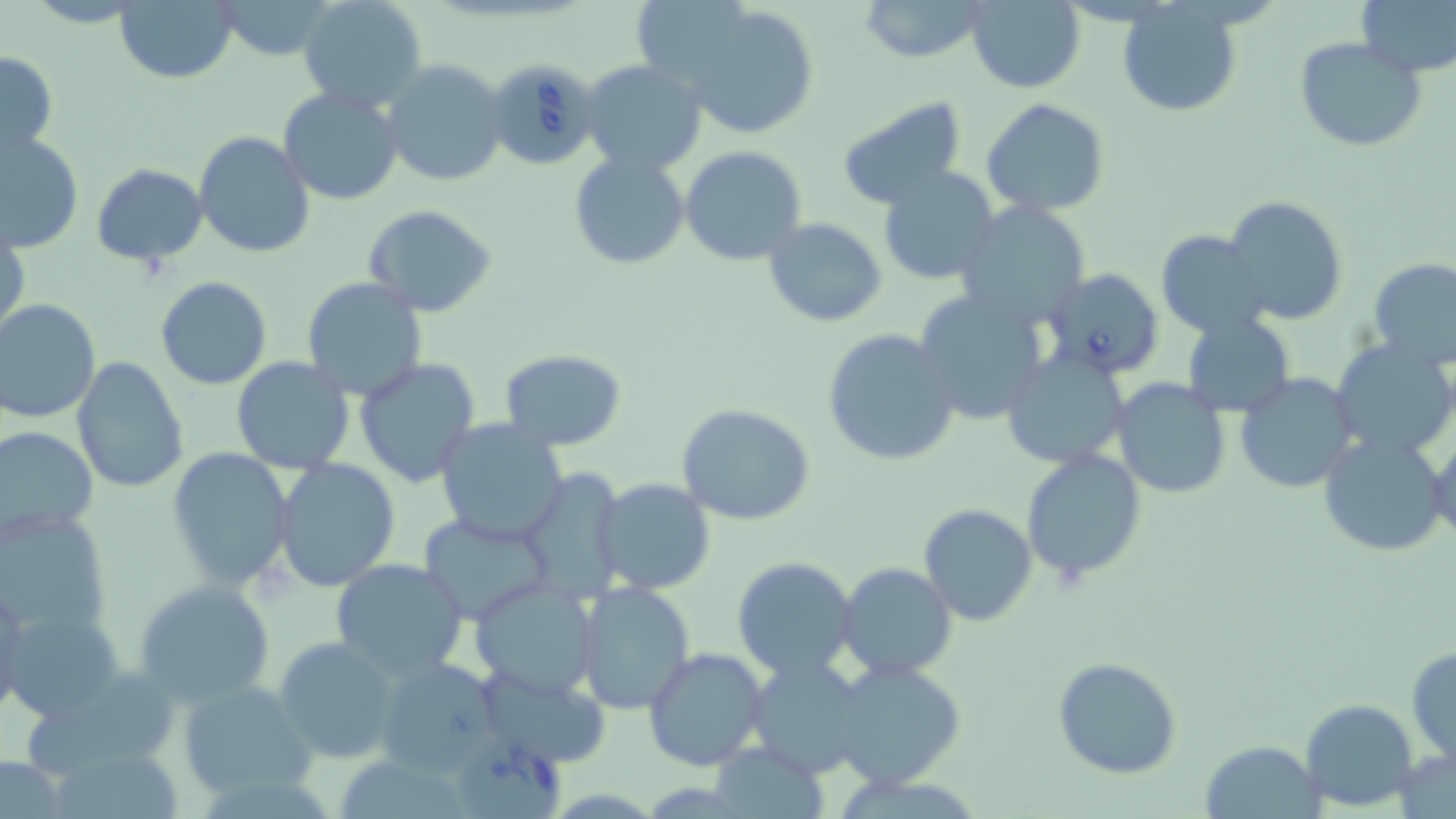
Approximate bounding boxes as named x1/y1/x2/y2 corners in pixels. Uninfected red blood cell locations: (x1=114, y1=0, x2=239, y2=83), (x1=214, y1=0, x2=340, y2=60), (x1=298, y1=0, x2=429, y2=114), (x1=859, y1=0, x2=989, y2=64), (x1=967, y1=0, x2=1086, y2=93), (x1=1358, y1=0, x2=1456, y2=77), (x1=1118, y1=4, x2=1242, y2=119), (x1=682, y1=5, x2=821, y2=138), (x1=1295, y1=37, x2=1426, y2=152), (x1=0, y1=48, x2=59, y2=162), (x1=380, y1=59, x2=508, y2=188), (x1=579, y1=59, x2=707, y2=177), (x1=279, y1=87, x2=403, y2=205), (x1=836, y1=97, x2=967, y2=211), (x1=981, y1=98, x2=1110, y2=219), (x1=193, y1=131, x2=314, y2=258), (x1=1, y1=133, x2=84, y2=253), (x1=681, y1=145, x2=807, y2=267), (x1=568, y1=150, x2=690, y2=268), (x1=92, y1=162, x2=207, y2=266), (x1=877, y1=165, x2=1001, y2=287), (x1=1224, y1=195, x2=1348, y2=324), (x1=955, y1=203, x2=1092, y2=326), (x1=361, y1=204, x2=496, y2=316), (x1=762, y1=217, x2=887, y2=328), (x1=1, y1=226, x2=28, y2=340), (x1=1156, y1=230, x2=1271, y2=339), (x1=1368, y1=256, x2=1456, y2=370), (x1=154, y1=276, x2=271, y2=389), (x1=302, y1=278, x2=429, y2=402), (x1=913, y1=290, x2=1049, y2=426), (x1=0, y1=299, x2=103, y2=422), (x1=1183, y1=313, x2=1295, y2=418), (x1=821, y1=327, x2=961, y2=466), (x1=1331, y1=339, x2=1456, y2=459), (x1=499, y1=349, x2=628, y2=452), (x1=1000, y1=350, x2=1132, y2=469), (x1=71, y1=357, x2=187, y2=493), (x1=354, y1=357, x2=482, y2=489), (x1=231, y1=358, x2=356, y2=474), (x1=1234, y1=373, x2=1361, y2=493), (x1=1111, y1=379, x2=1232, y2=498), (x1=677, y1=403, x2=816, y2=526), (x1=434, y1=417, x2=569, y2=546), (x1=0, y1=426, x2=99, y2=542), (x1=1317, y1=432, x2=1450, y2=558), (x1=1429, y1=434, x2=1456, y2=544), (x1=169, y1=448, x2=295, y2=592), (x1=1022, y1=449, x2=1147, y2=583), (x1=272, y1=458, x2=401, y2=591), (x1=516, y1=469, x2=627, y2=602), (x1=591, y1=478, x2=716, y2=596), (x1=0, y1=503, x2=111, y2=639), (x1=919, y1=503, x2=1037, y2=626), (x1=418, y1=512, x2=554, y2=624), (x1=731, y1=556, x2=857, y2=680), (x1=330, y1=559, x2=470, y2=679), (x1=835, y1=563, x2=957, y2=680), (x1=133, y1=578, x2=274, y2=705), (x1=467, y1=580, x2=602, y2=701), (x1=0, y1=581, x2=25, y2=723), (x1=574, y1=581, x2=697, y2=713), (x1=3, y1=606, x2=126, y2=723), (x1=273, y1=635, x2=403, y2=764), (x1=643, y1=646, x2=768, y2=772), (x1=1407, y1=648, x2=1455, y2=761), (x1=371, y1=653, x2=501, y2=775), (x1=747, y1=655, x2=872, y2=778), (x1=1052, y1=657, x2=1182, y2=778), (x1=830, y1=659, x2=964, y2=788), (x1=27, y1=662, x2=185, y2=779), (x1=470, y1=662, x2=613, y2=770), (x1=176, y1=677, x2=315, y2=803), (x1=1301, y1=698, x2=1418, y2=810), (x1=1201, y1=738, x2=1322, y2=817), (x1=710, y1=745, x2=832, y2=818), (x1=56, y1=752, x2=181, y2=819), (x1=343, y1=753, x2=466, y2=819), (x1=0, y1=754, x2=72, y2=819). Babesia divergens-infected red blood cell locations: (x1=483, y1=59, x2=603, y2=170), (x1=1041, y1=268, x2=1165, y2=378), (x1=452, y1=744, x2=563, y2=819). Slide-level diagnosis: Babesia divergens. Optical microscopy. One field of a larger specimen. May-Grünwald-Giemsa-stained preparation. 1000x magnification. Thin blood film. Image is 1456×819 pixels.